Describe the morphology of the red blood cells.
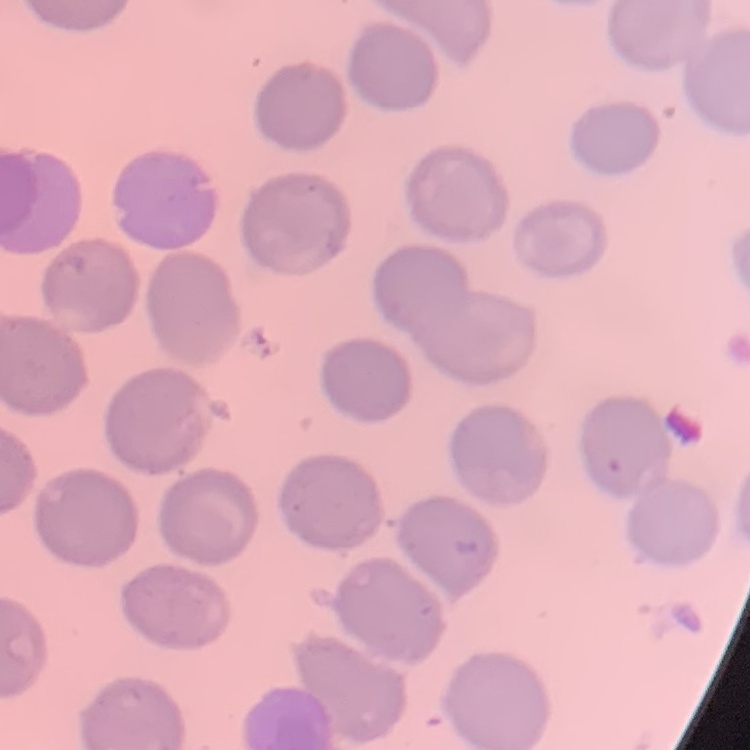

No rouleaux formation.

Field's or Giemsa stain. Thin peripheral smear. One tile cut from a larger photomicrograph.